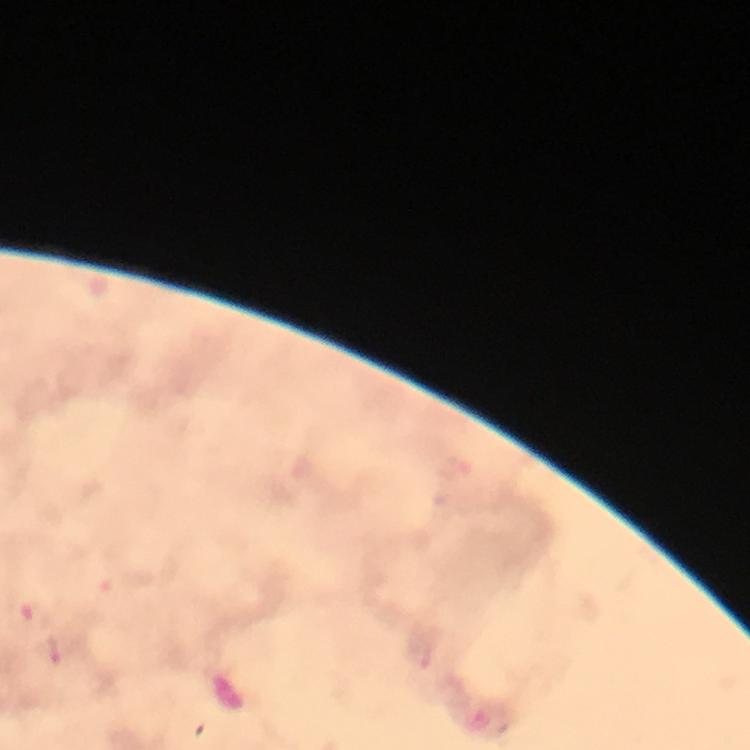

stain: Giemsa
context: from a malaria diagnostic workup
malaria_parasite_locations: 'approximate centers as {x, y} in pixels: {35, 615}, {48, 654}'
preparation: thick blood film
magnification: 100x
cropped_from: a single field of view
immersion_oil: applied
image_size: 750×750 pixels
capture: smartphone camera through the microscope